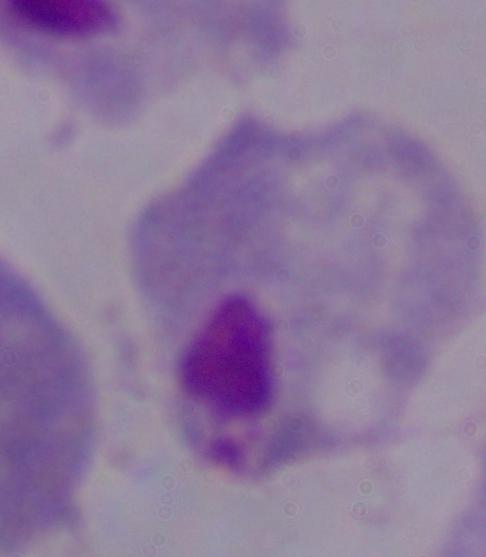
Captured at 1000x magnification. A trichomonad is seen. Photomicrograph.